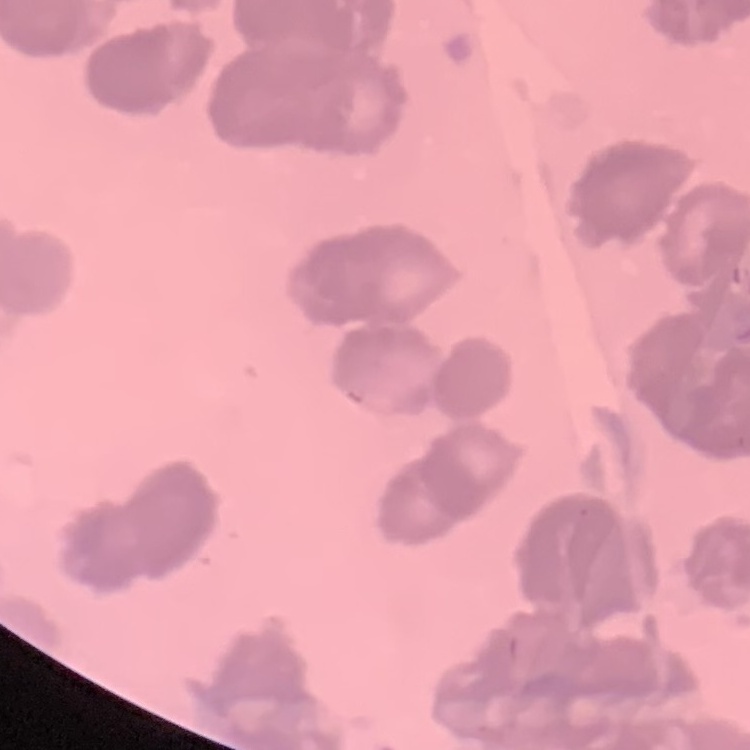
{
  "red_blood_cell_morphology": "rouleaux formation",
  "stain": "Field's or Giemsa",
  "preparation": "thin blood film",
  "image_type": "one tile cut from a larger photomicrograph"
}